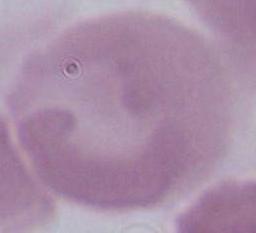 1000x magnification. Micrograph. An erythrocyte is shown.